Name the parasite shown.
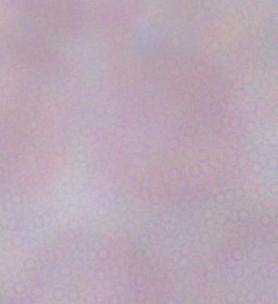
This is a trypanosome.

Summary:
  - Modality: photomicrograph
  - Magnification: 1000x